Locate every Plasmodium falciparum-infected red blood cell.
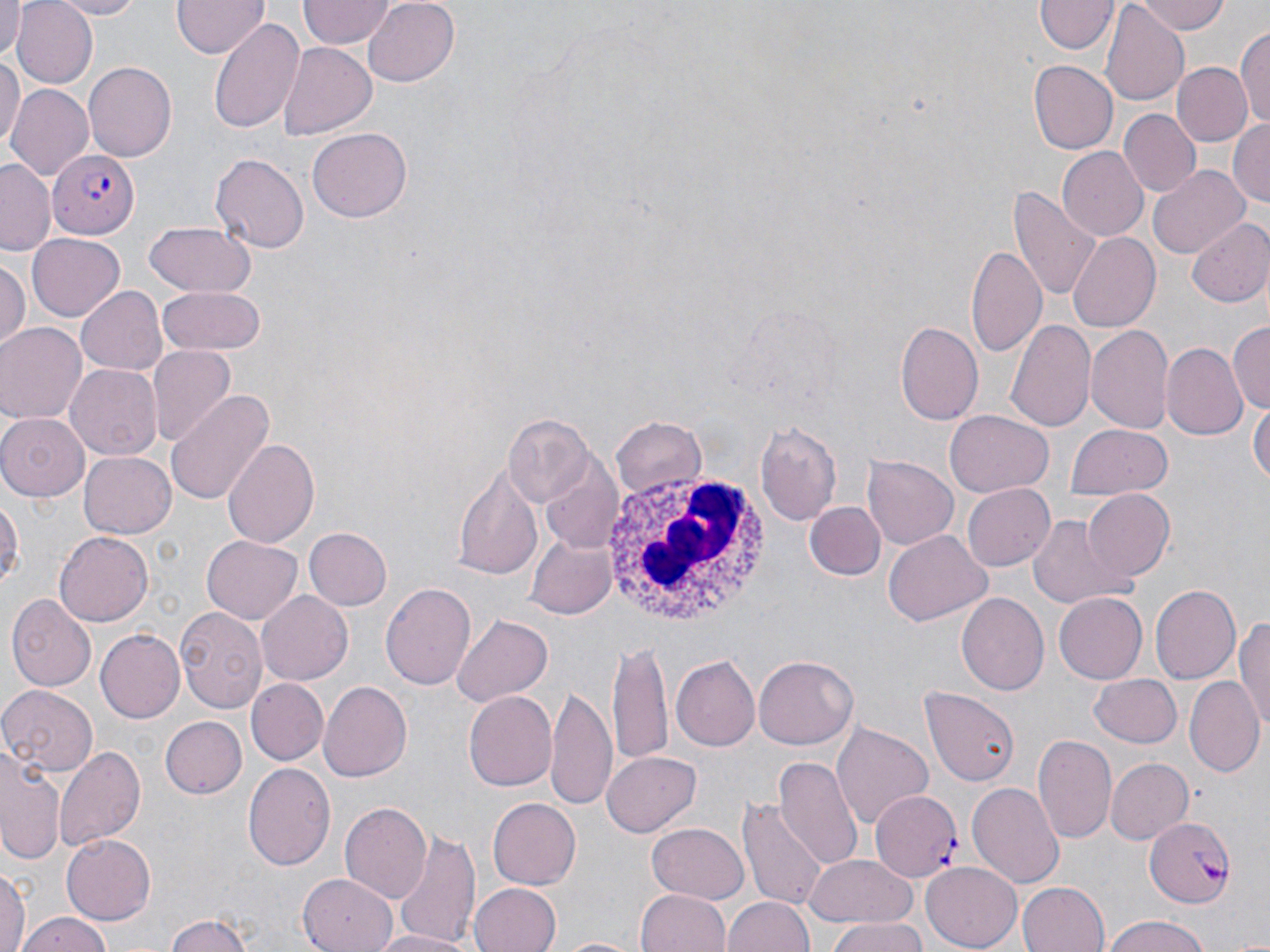
Approximate bounding boxes as [x1, y1, x2, y2] in pixels.
Plasmodium falciparum-infected red blood cells: [49, 147, 138, 239], [869, 791, 963, 878], [1144, 815, 1236, 907].

Summary:
  - White blood cell locations: [603, 473, 771, 631]
  - Uninfected red blood cell locations: [0, 0, 26, 61], [12, 0, 98, 88], [47, 0, 146, 17], [170, 0, 267, 59], [299, 0, 392, 49], [361, 0, 460, 88], [1130, 0, 1229, 35], [1035, 2, 1116, 56], [1102, 7, 1188, 106], [209, 19, 305, 132], [1235, 27, 1269, 129], [277, 42, 375, 140], [0, 55, 22, 153], [1027, 60, 1117, 154], [1173, 61, 1252, 148], [82, 62, 177, 162], [7, 85, 92, 180], [1120, 108, 1200, 197], [1227, 118, 1270, 207], [308, 125, 410, 220], [1057, 147, 1148, 242], [211, 153, 309, 254], [1, 160, 58, 256], [1149, 164, 1249, 260], [1013, 183, 1104, 305], [1188, 217, 1270, 309], [142, 222, 255, 297], [1067, 231, 1160, 334], [27, 233, 126, 321], [968, 243, 1049, 358], [0, 258, 28, 352], [75, 286, 166, 377], [158, 289, 265, 355], [1007, 319, 1097, 435], [898, 320, 984, 425], [1086, 321, 1174, 434], [1228, 321, 1269, 412], [0, 325, 85, 425], [1163, 343, 1247, 440], [148, 347, 233, 445], [65, 364, 163, 460], [164, 390, 274, 505], [1250, 394, 1269, 495], [943, 411, 1052, 496], [0, 414, 88, 502], [502, 414, 594, 505], [610, 416, 708, 500], [755, 420, 844, 525], [1066, 423, 1173, 503], [222, 438, 320, 547], [79, 452, 176, 538], [539, 456, 623, 555], [864, 456, 958, 549], [452, 464, 542, 580], [962, 481, 1056, 569], [1084, 489, 1174, 581], [0, 492, 23, 591], [805, 502, 885, 581], [1026, 512, 1135, 611], [306, 527, 392, 609], [882, 529, 991, 626], [53, 530, 152, 627], [526, 534, 618, 617], [200, 536, 304, 625], [381, 583, 476, 690], [1151, 584, 1241, 685], [257, 590, 353, 684], [958, 593, 1049, 697], [1055, 593, 1148, 683], [8, 594, 97, 690], [173, 605, 268, 712], [451, 614, 552, 706], [1234, 614, 1269, 734], [95, 629, 185, 722], [612, 639, 675, 770], [672, 656, 759, 750], [755, 656, 857, 749], [1088, 674, 1182, 747], [1187, 675, 1264, 779], [248, 678, 329, 766], [319, 682, 412, 782], [0, 684, 100, 778], [922, 684, 1020, 785], [547, 685, 617, 815], [464, 690, 558, 792], [161, 716, 248, 799], [832, 722, 933, 830], [1032, 735, 1117, 847], [55, 745, 145, 850], [0, 749, 65, 866], [603, 751, 701, 836], [775, 756, 863, 872], [1105, 757, 1194, 846], [242, 762, 336, 869], [967, 779, 1064, 888], [488, 797, 581, 889], [737, 797, 825, 911], [340, 803, 432, 905], [646, 823, 749, 905], [394, 831, 480, 945], [61, 833, 156, 924], [807, 855, 919, 929], [921, 862, 1024, 949], [1, 869, 30, 950], [300, 872, 394, 951], [1018, 880, 1111, 952], [469, 882, 560, 952], [638, 888, 732, 952], [724, 895, 816, 952], [14, 912, 115, 952], [163, 914, 262, 952], [1101, 915, 1211, 952], [826, 923, 932, 952], [369, 930, 476, 952], [551, 936, 645, 952]
  - Slide-level diagnosis: Plasmodium falciparum
  - Magnification: 1000x
  - Stain: May-Grünwald-Giemsa
  - Modality: optical microscopy
  - Field of view: single
  - Image size: 1270×952 pixels
  - Preparation: thin blood smear